Report the malaria status of this cell.
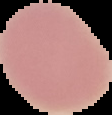

It is uninfected.

Summary:
  - Image type: segmented cell region on a black background
  - Preparation: thin blood smear
  - Image size: 112×115 pixels